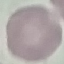 Malaria status: uninfected. Automatically extracted cell patch, resized to 64 × 64 pixels. Thin blood film. Giemsa stain. Photographed with a smartphone camera at the microscope eyepiece.